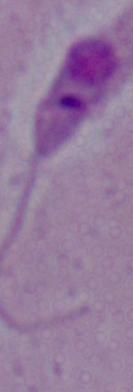

{
  "magnification": "1000x",
  "modality": "micrograph",
  "identification": "Leishmania"
}